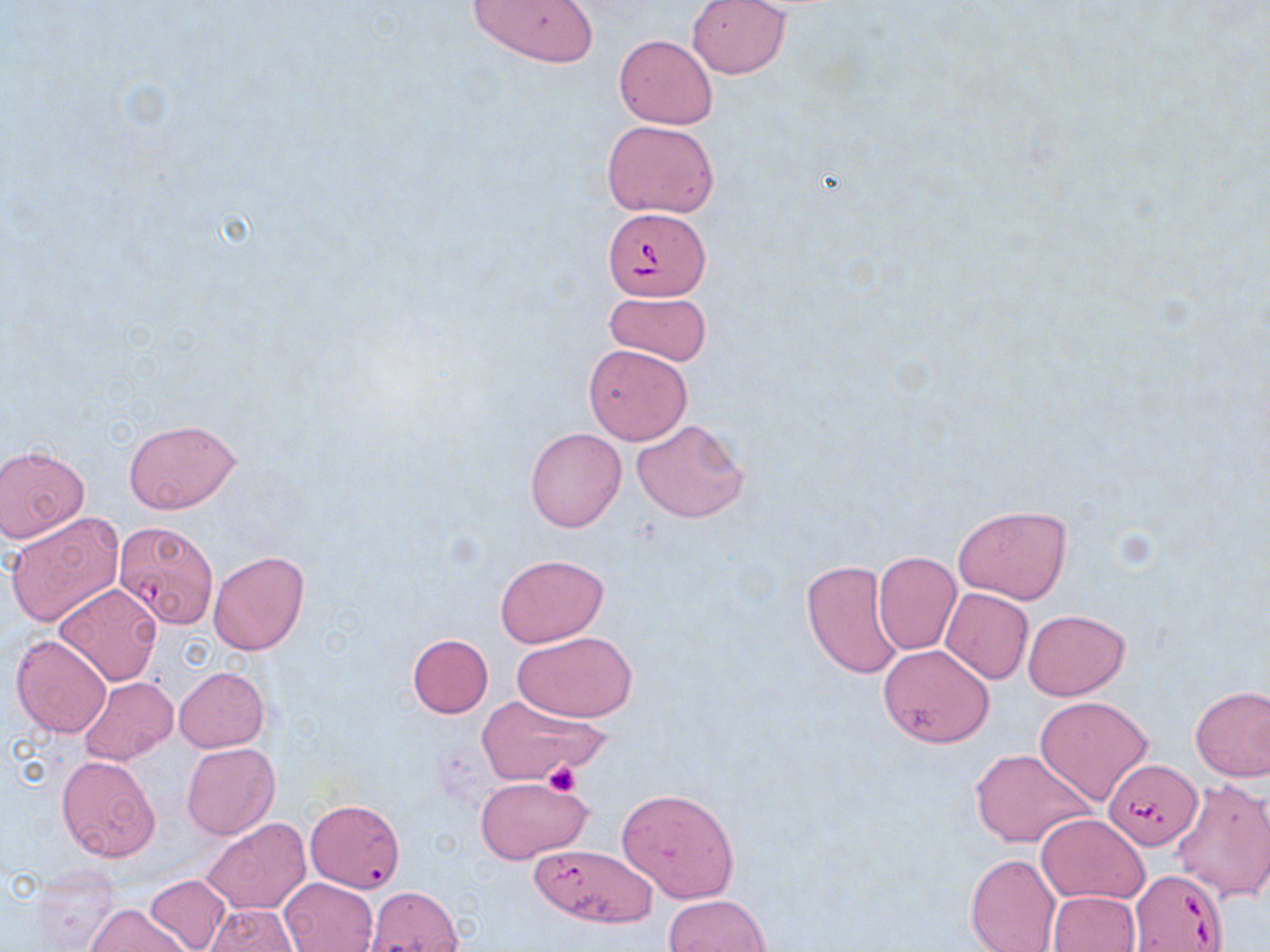

Summary:
  - Coordinate format: approximate bounding boxes as named x1/y1/x2/y2 corners in pixels
  - Babesia divergens-infected red blood cell locations: (x1=603, y1=206, x2=712, y2=300), (x1=114, y1=525, x2=211, y2=631), (x1=1104, y1=761, x2=1198, y2=849), (x1=1129, y1=870, x2=1227, y2=951)
  - Platelet locations: (x1=543, y1=762, x2=581, y2=797)
  - Uninfected red blood cell locations: (x1=468, y1=0, x2=599, y2=69), (x1=687, y1=0, x2=790, y2=79), (x1=614, y1=35, x2=716, y2=130), (x1=602, y1=119, x2=720, y2=219), (x1=604, y1=290, x2=711, y2=367), (x1=583, y1=343, x2=693, y2=445), (x1=631, y1=418, x2=749, y2=524), (x1=123, y1=419, x2=240, y2=514), (x1=524, y1=427, x2=626, y2=532), (x1=0, y1=445, x2=89, y2=543), (x1=953, y1=504, x2=1073, y2=605), (x1=6, y1=510, x2=123, y2=627), (x1=208, y1=550, x2=310, y2=656), (x1=873, y1=552, x2=962, y2=656), (x1=495, y1=554, x2=609, y2=647), (x1=801, y1=560, x2=904, y2=680), (x1=54, y1=582, x2=162, y2=686), (x1=941, y1=587, x2=1033, y2=684), (x1=1022, y1=609, x2=1129, y2=699), (x1=513, y1=630, x2=638, y2=723), (x1=10, y1=633, x2=112, y2=738), (x1=406, y1=633, x2=493, y2=717), (x1=878, y1=644, x2=995, y2=747), (x1=174, y1=666, x2=270, y2=753), (x1=79, y1=676, x2=177, y2=766), (x1=1190, y1=685, x2=1270, y2=782), (x1=474, y1=694, x2=610, y2=786), (x1=1035, y1=695, x2=1153, y2=806), (x1=182, y1=742, x2=280, y2=839), (x1=969, y1=747, x2=1097, y2=848), (x1=57, y1=755, x2=160, y2=862), (x1=473, y1=776, x2=595, y2=865), (x1=1170, y1=778, x2=1270, y2=903), (x1=618, y1=788, x2=740, y2=902), (x1=305, y1=799, x2=405, y2=892), (x1=1036, y1=814, x2=1149, y2=904), (x1=202, y1=818, x2=310, y2=916), (x1=528, y1=843, x2=657, y2=928), (x1=965, y1=852, x2=1061, y2=952), (x1=32, y1=864, x2=121, y2=951), (x1=145, y1=873, x2=234, y2=952), (x1=281, y1=878, x2=377, y2=952), (x1=365, y1=887, x2=464, y2=951), (x1=1048, y1=890, x2=1140, y2=952), (x1=663, y1=894, x2=772, y2=952), (x1=86, y1=902, x2=193, y2=952), (x1=205, y1=904, x2=298, y2=951)
  - Slide-level diagnosis: Babesia divergens
  - Stain: May-Grünwald-Giemsa
  - Magnification: 1000x
  - Modality: optical microscopy
  - Image size: 1270×952 pixels
  - Preparation: thin blood film
  - Field of view: single